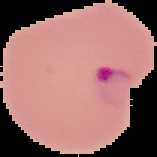
preparation: thin blood film
image_type: segmented cell region with the area outside set to black
image_size: 157×157 pixels
malaria_status: parasitized